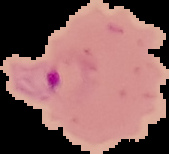
preparation = thin blood film
malaria status = parasitized
image size = 169×154 pixels
image type = cell region segmented out of the field of view; surrounding area masked to black